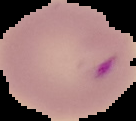
preparation = thin blood film
image size = 136×121 pixels
result = Plasmodium parasites detected
image type = segmented cell region on a black background